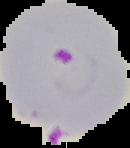

Image is 130×148 pixels. From a thin blood smear. Result: malaria parasites identified. Segmented cell region on a black background.